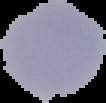

malaria status = uninfected
preparation = thin blood smear
image type = segmented cell region with the area outside set to black
image size = 106×103 pixels